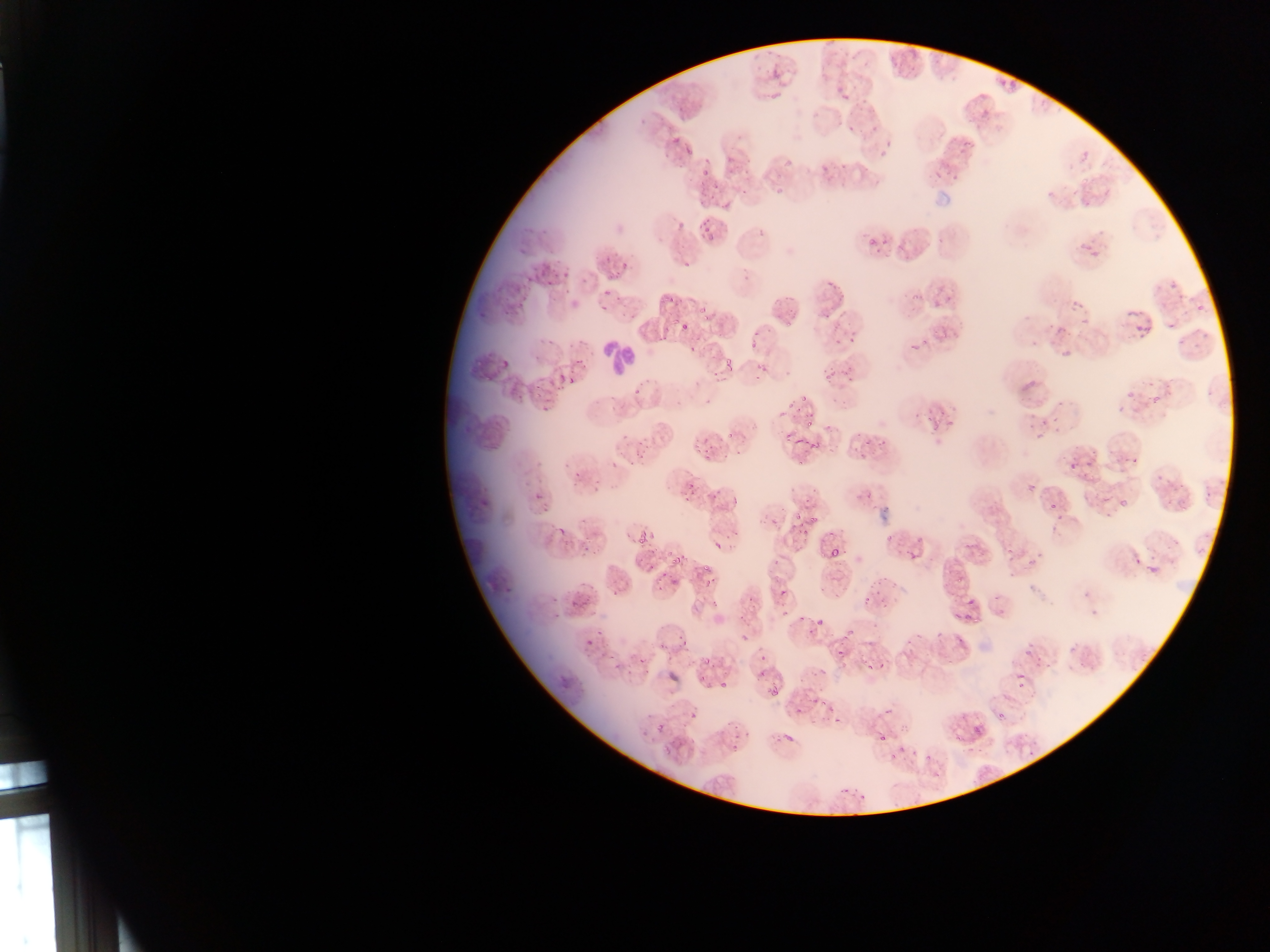

Approximate bounding boxes as (left, top, right, bottom) in pixels. Malaria parasite locations: (769, 71, 779, 83), (996, 77, 1008, 90), (833, 82, 845, 93), (768, 91, 781, 100), (841, 91, 850, 102), (847, 126, 856, 135), (870, 128, 878, 134), (669, 132, 686, 145), (884, 141, 893, 148), (680, 144, 696, 156), (879, 149, 891, 160), (785, 156, 796, 166), (820, 158, 831, 170), (699, 167, 714, 180), (778, 187, 782, 196), (1045, 188, 1054, 197), (1071, 189, 1081, 197), (702, 218, 711, 230), (706, 231, 717, 241), (880, 233, 890, 250), (1077, 235, 1088, 250), (866, 240, 876, 247), (517, 248, 530, 255), (1090, 248, 1103, 262), (600, 257, 613, 263), (616, 260, 628, 276), (538, 261, 551, 277), (681, 261, 690, 268), (606, 270, 615, 279), (563, 273, 572, 287), (523, 276, 532, 284), (827, 279, 834, 289), (544, 281, 554, 288), (602, 290, 611, 300), (907, 291, 922, 302), (944, 294, 958, 302), (517, 295, 531, 321), (666, 297, 674, 306), (932, 297, 942, 307), (1071, 297, 1083, 315), (1192, 297, 1211, 320), (698, 301, 712, 312), (498, 303, 514, 321), (597, 307, 606, 313), (703, 312, 715, 322), (1126, 312, 1154, 345), (823, 313, 833, 324), (1080, 314, 1089, 326), (675, 320, 690, 329), (1168, 324, 1179, 332), (1048, 326, 1067, 336), (941, 327, 950, 339), (546, 337, 558, 348), (848, 337, 859, 345), (919, 337, 933, 349), (748, 338, 760, 350), (906, 339, 918, 354), (1061, 348, 1069, 361), (720, 352, 740, 367), (573, 356, 584, 367), (500, 358, 511, 368), (828, 365, 839, 378), (560, 370, 581, 388), (826, 372, 833, 381), (567, 375, 582, 389), (633, 386, 644, 396), (607, 391, 616, 401), (1126, 391, 1133, 400), (799, 392, 803, 401), (1151, 392, 1161, 405), (1056, 397, 1068, 408), (540, 404, 554, 418), (786, 404, 798, 412), (1051, 413, 1061, 423), (1040, 414, 1045, 425), (925, 415, 935, 426), (941, 415, 953, 430), (802, 419, 814, 434), (1056, 424, 1063, 432), (726, 431, 738, 438), (784, 433, 794, 443), (1036, 433, 1043, 441), (621, 435, 630, 444), (860, 435, 873, 448), (810, 436, 822, 449), (695, 438, 706, 453), (633, 442, 644, 460), (706, 445, 717, 461), (606, 455, 620, 467), (1128, 456, 1146, 469), (798, 457, 811, 469), (624, 458, 636, 470), (1071, 460, 1079, 472), (1086, 460, 1095, 468), (573, 463, 588, 477), (1152, 471, 1164, 481), (589, 477, 603, 491), (688, 478, 701, 490), (1026, 480, 1037, 491), (533, 490, 546, 503), (1204, 490, 1213, 500), (1050, 495, 1063, 509), (1179, 498, 1189, 513), (1118, 499, 1130, 506), (792, 512, 806, 528), (807, 513, 818, 525), (770, 517, 780, 524), (554, 521, 569, 537), (795, 523, 806, 535), (633, 533, 648, 543), (885, 533, 896, 541), (578, 538, 596, 558), (713, 540, 723, 548), (830, 546, 840, 563), (1003, 546, 1017, 557), (1036, 551, 1046, 562), (905, 553, 922, 565), (672, 555, 682, 564), (646, 556, 658, 574), (1028, 559, 1036, 569), (1130, 560, 1141, 565), (1147, 562, 1158, 575), (694, 563, 710, 575), (656, 566, 673, 584), (956, 574, 966, 587), (502, 576, 519, 594), (704, 576, 715, 588), (872, 580, 882, 595), (612, 584, 625, 600), (779, 586, 791, 599), (551, 593, 559, 608), (864, 595, 872, 606), (954, 597, 982, 627), (548, 606, 562, 620), (815, 614, 830, 625), (842, 621, 860, 638), (934, 632, 941, 640), (581, 635, 598, 651), (741, 637, 751, 645), (660, 640, 673, 655), (904, 640, 911, 648), (1069, 644, 1078, 655), (605, 645, 621, 661), (834, 647, 847, 658), (1021, 647, 1031, 656), (702, 651, 713, 667), (865, 654, 885, 670), (757, 655, 770, 664), (758, 668, 769, 684), (1012, 669, 1032, 692), (719, 676, 731, 692), (770, 685, 786, 700), (816, 698, 831, 704), (881, 701, 890, 714), (827, 703, 839, 715), (795, 709, 802, 717), (996, 710, 1012, 720), (834, 715, 840, 726), (655, 721, 667, 736), (781, 722, 800, 742), (972, 725, 984, 735), (879, 736, 886, 744), (729, 739, 743, 755), (897, 745, 906, 751), (909, 751, 918, 760), (886, 754, 897, 764), (926, 756, 935, 765) | approximate (x, y) pixel centers of objects too small to bound: (742, 193), (788, 326), (765, 370), (957, 741). Leukocyte locations: (605, 336, 641, 378). One field of view. Mobile-phone photograph taken through the microscope. Image is 1270×952 pixels. Thin blood smear. Sample from Ghana.